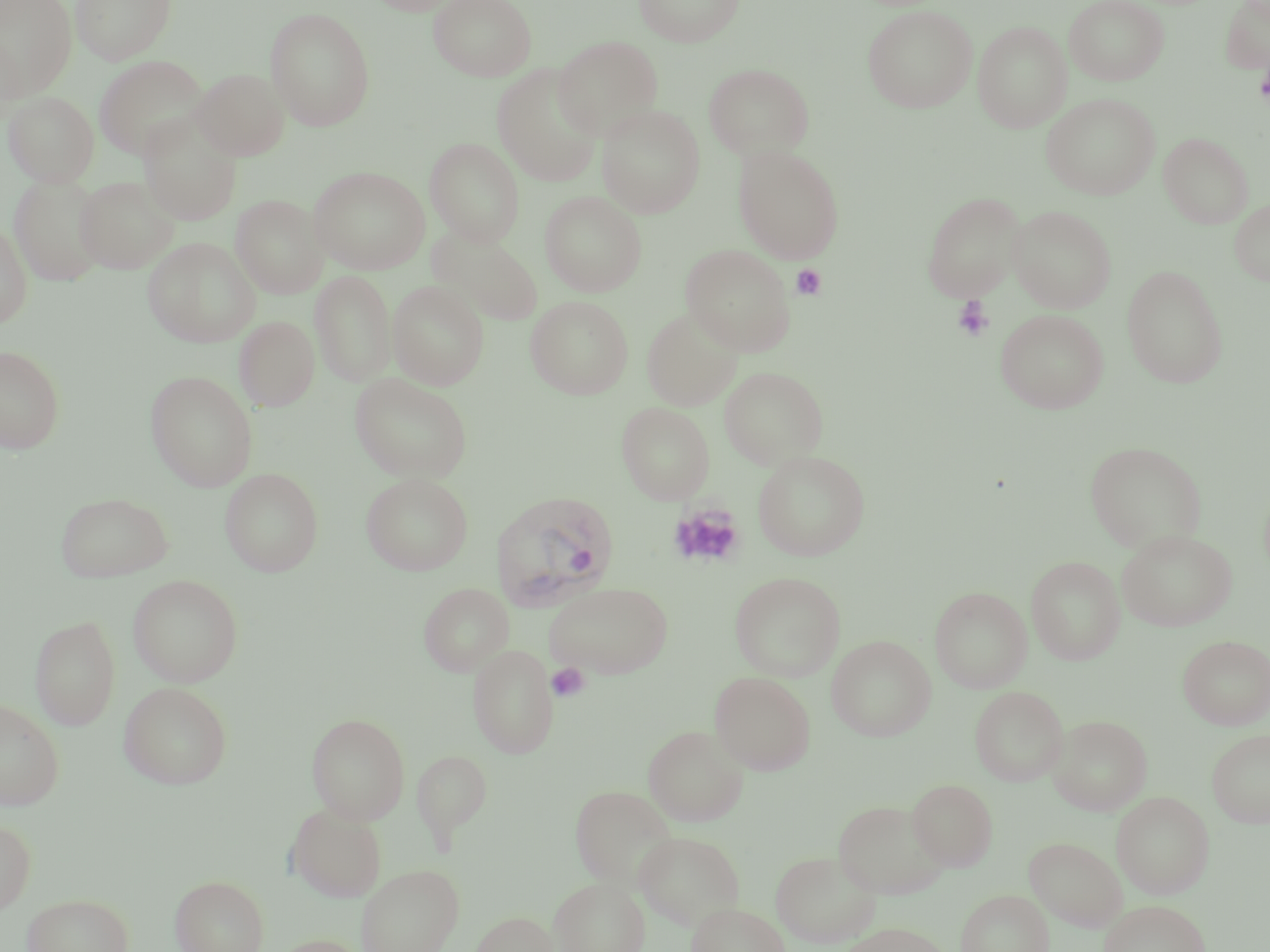
Approximate bounding boxes as [x1, y1, x2, y2] in pixels. Plasmodium vivax-infected red blood cell locations: [489, 490, 619, 612]. Platelet locations: [1255, 52, 1270, 110], [791, 264, 826, 300], [952, 296, 994, 342], [668, 504, 745, 568], [547, 663, 590, 702]. Uninfected red blood cell locations: [0, 0, 78, 98], [70, 0, 177, 65], [367, 0, 467, 15], [429, 0, 537, 82], [634, 0, 744, 47], [1064, 0, 1169, 85], [1220, 1, 1270, 74], [861, 4, 978, 113], [264, 7, 376, 131], [973, 22, 1071, 132], [0, 35, 23, 126], [553, 36, 663, 139], [94, 55, 209, 160], [703, 62, 814, 161], [492, 64, 604, 187], [191, 68, 290, 160], [3, 91, 99, 187], [1041, 93, 1160, 200], [596, 104, 705, 218], [138, 113, 242, 226], [1159, 132, 1253, 228], [425, 137, 525, 246], [733, 144, 845, 264], [309, 166, 431, 274], [9, 174, 108, 286], [75, 176, 179, 274], [540, 191, 647, 296], [921, 192, 1025, 301], [231, 194, 329, 299], [1230, 198, 1270, 286], [1009, 205, 1116, 313], [0, 220, 32, 329], [429, 227, 543, 326], [143, 237, 260, 348], [681, 245, 795, 355], [1121, 264, 1229, 388], [310, 270, 396, 388], [388, 280, 490, 390], [526, 295, 634, 399], [641, 307, 744, 410], [996, 308, 1109, 413], [234, 316, 320, 411], [0, 345, 65, 454], [719, 366, 828, 469], [145, 371, 258, 491], [350, 373, 472, 482], [616, 402, 715, 504], [1084, 440, 1207, 553], [753, 450, 871, 561], [220, 468, 323, 576], [361, 473, 473, 575], [55, 492, 174, 582], [1117, 529, 1237, 631], [1026, 556, 1126, 664], [730, 572, 845, 682], [128, 574, 243, 687], [544, 581, 673, 680], [418, 582, 513, 676], [930, 586, 1032, 693], [30, 614, 120, 730], [1178, 635, 1270, 730], [1197, 635, 1270, 828], [827, 636, 936, 741], [468, 643, 558, 757], [710, 672, 816, 775], [118, 681, 233, 789], [970, 686, 1068, 786], [0, 698, 64, 810], [307, 713, 410, 825], [1049, 715, 1153, 815], [643, 725, 748, 827], [1207, 728, 1270, 828], [411, 749, 492, 843], [907, 778, 998, 870], [570, 785, 678, 889], [1111, 791, 1215, 898], [832, 800, 950, 899], [286, 803, 387, 902], [0, 819, 36, 916], [634, 830, 745, 929], [1025, 836, 1126, 931], [770, 850, 881, 948], [357, 864, 464, 952], [170, 875, 269, 952], [549, 877, 650, 952], [956, 889, 1054, 952], [21, 893, 134, 952], [1099, 899, 1210, 952], [686, 902, 790, 952], [469, 911, 559, 951], [836, 922, 953, 952], [269, 934, 368, 952]. Slide-level diagnosis: Plasmodium vivax. Captured at 1000x magnification. Optical microscopy. Thin blood film. Single field of view. May-Grünwald-Giemsa stain. Image is 1270×952 pixels.